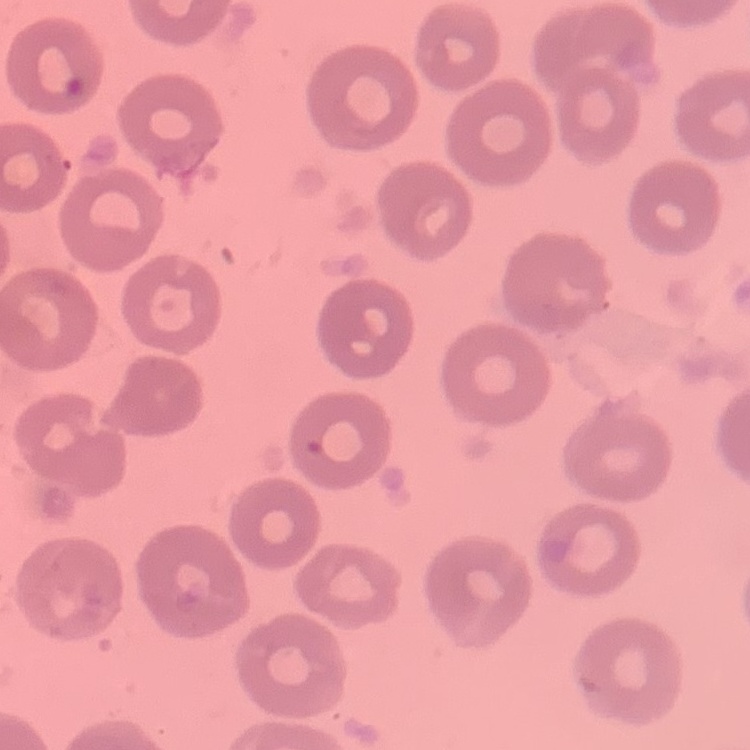

The red blood cells exhibit no rouleaux formation. Field's or Giemsa stain. Thin blood smear. Square crop of a larger photomicrograph.